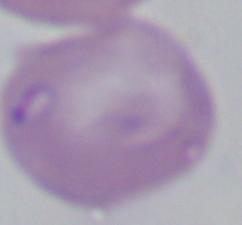 A Babesia parasite is shown. Micrograph. 1000x magnification.